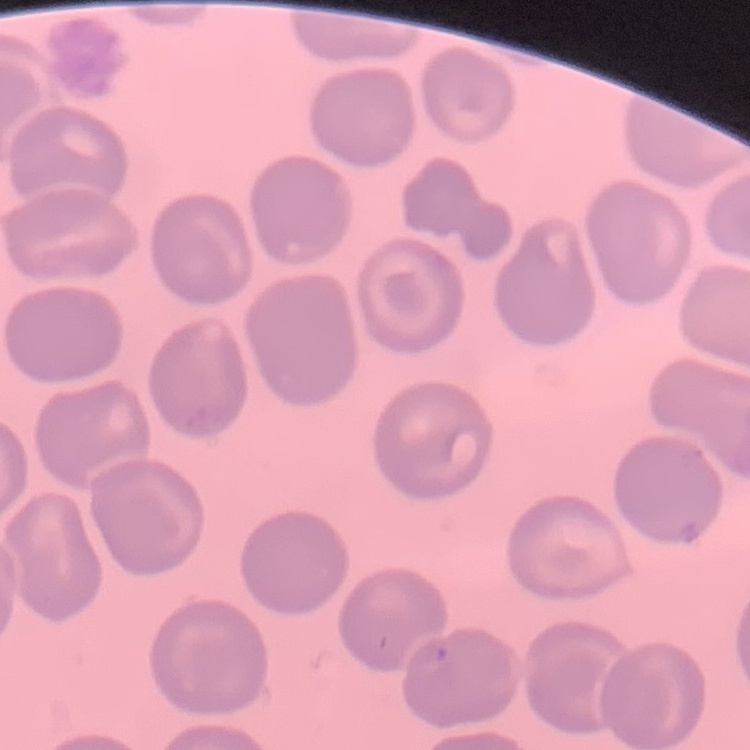 The red blood cells exhibit no rouleaux formation. Stained with either Field's or Giemsa. Thin blood smear. Square crop of a larger photomicrograph.